Assess the morphology of the erythrocytes.
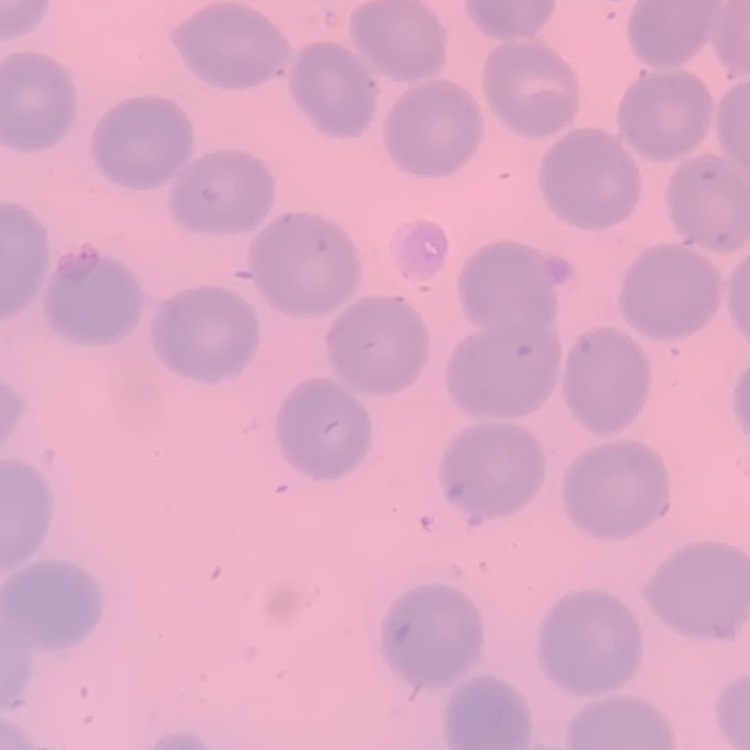
They show no rouleaux formation.

Summary:
  - Image type: one tile cut from a larger photomicrograph
  - Preparation: thin blood film
  - Stain: Field's or Giemsa